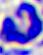

modality = photomicrograph
magnification = 400x
identification = white blood cell